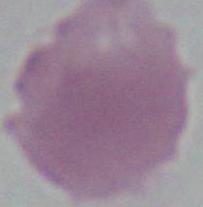

Summary:
  - Magnification: 1000x
  - Modality: photomicrograph
  - Identification: red blood cell